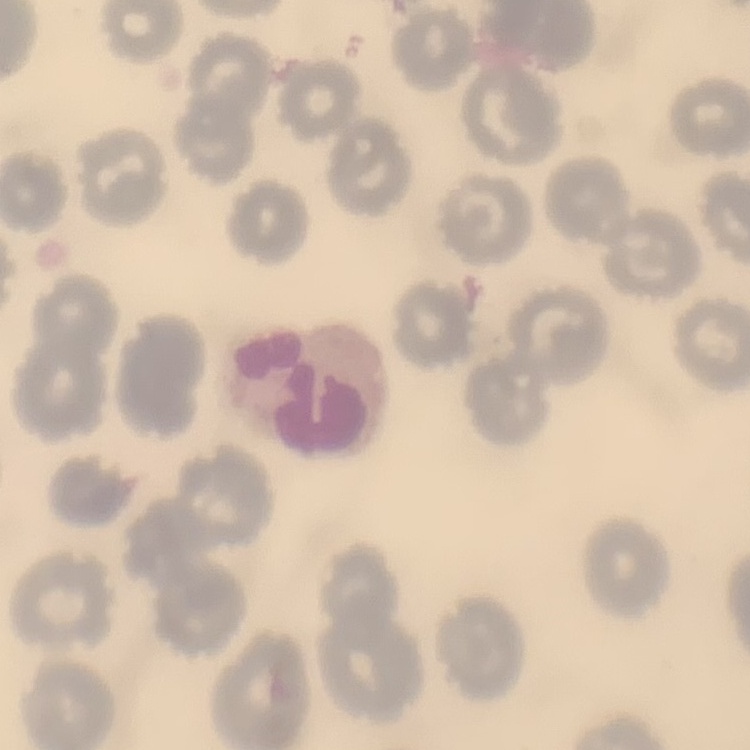
erythrocyte morphology = no rouleaux formation
stain = Field's or Giemsa
image type = square crop of a larger photomicrograph
preparation = thin peripheral smear